Locate platelets.
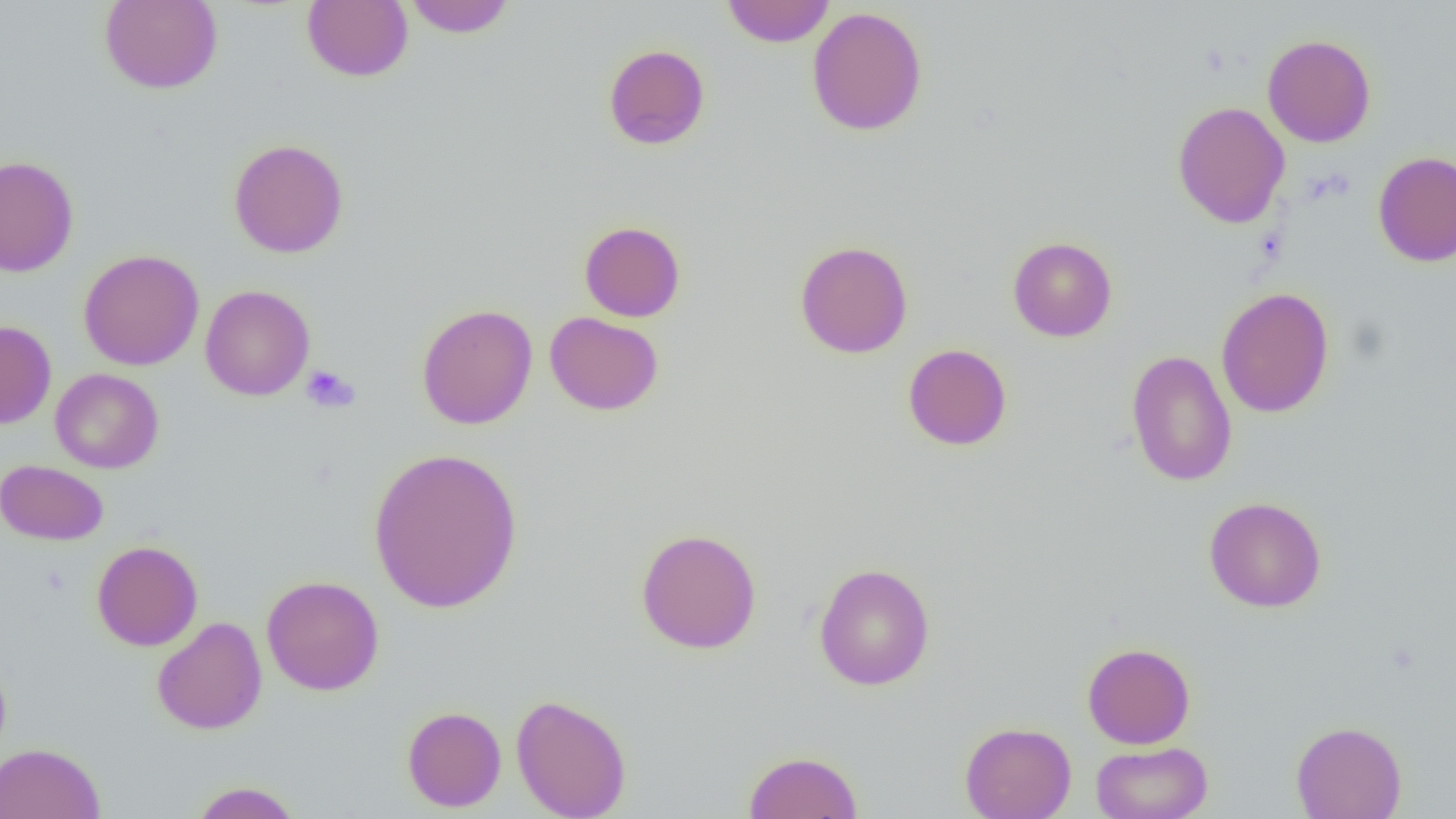

Approximate bounding boxes as (x1,y1)-(x2,y2) corner pairs in pixels.
Platelets: (300,365)-(360,414).

{
  "slide_level_diagnosis": "negative for blood parasites",
  "field_of_view": "one of a larger specimen",
  "magnification": "1000x",
  "uninfected_red_blood_cell_locations": "approximate bounding boxes as (x1,y1)-(x2,y2) corner pairs in pixels: (403,0)-(516,37), (721,0)-(835,48), (99,1)-(223,94), (303,1)-(413,82), (806,6)-(928,136), (1262,34)-(1376,148), (603,44)-(710,150), (1172,100)-(1290,228), (229,138)-(349,258), (1373,150)-(1456,267), (0,154)-(79,277), (579,220)-(686,322), (1007,236)-(1117,342), (795,240)-(913,358), (78,249)-(205,371), (199,284)-(315,401), (1216,287)-(1335,418), (416,303)-(538,430), (544,311)-(664,415), (0,320)-(57,429), (903,343)-(1012,451), (1126,350)-(1237,487), (50,368)-(163,473), (367,446)-(524,615), (0,460)-(108,545), (1204,496)-(1326,612), (635,527)-(762,654), (91,540)-(203,651), (814,562)-(935,691), (261,575)-(384,696), (152,616)-(267,734), (1082,642)-(1196,749), (0,654)-(12,764), (511,693)-(632,819), (402,706)-(506,812), (1291,720)-(1407,819), (960,721)-(1076,819), (1091,740)-(1213,819), (0,743)-(105,819), (743,750)-(863,818), (188,781)-(304,819)",
  "preparation": "thin blood film",
  "image_size": "1456×819 pixels",
  "modality": "light microscopy"
}